Classify this cell by malaria status.
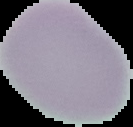
It is uninfected.

{
  "image_size": "133×127 pixels",
  "preparation": "thin blood film",
  "image_type": "segmented cell region on a black background"
}